Assess this cell for malaria.
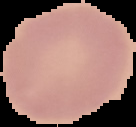

Uninfected.

Summary:
  - Image type: segmented cell region on a black background
  - Image size: 136×127 pixels
  - Preparation: thin blood film